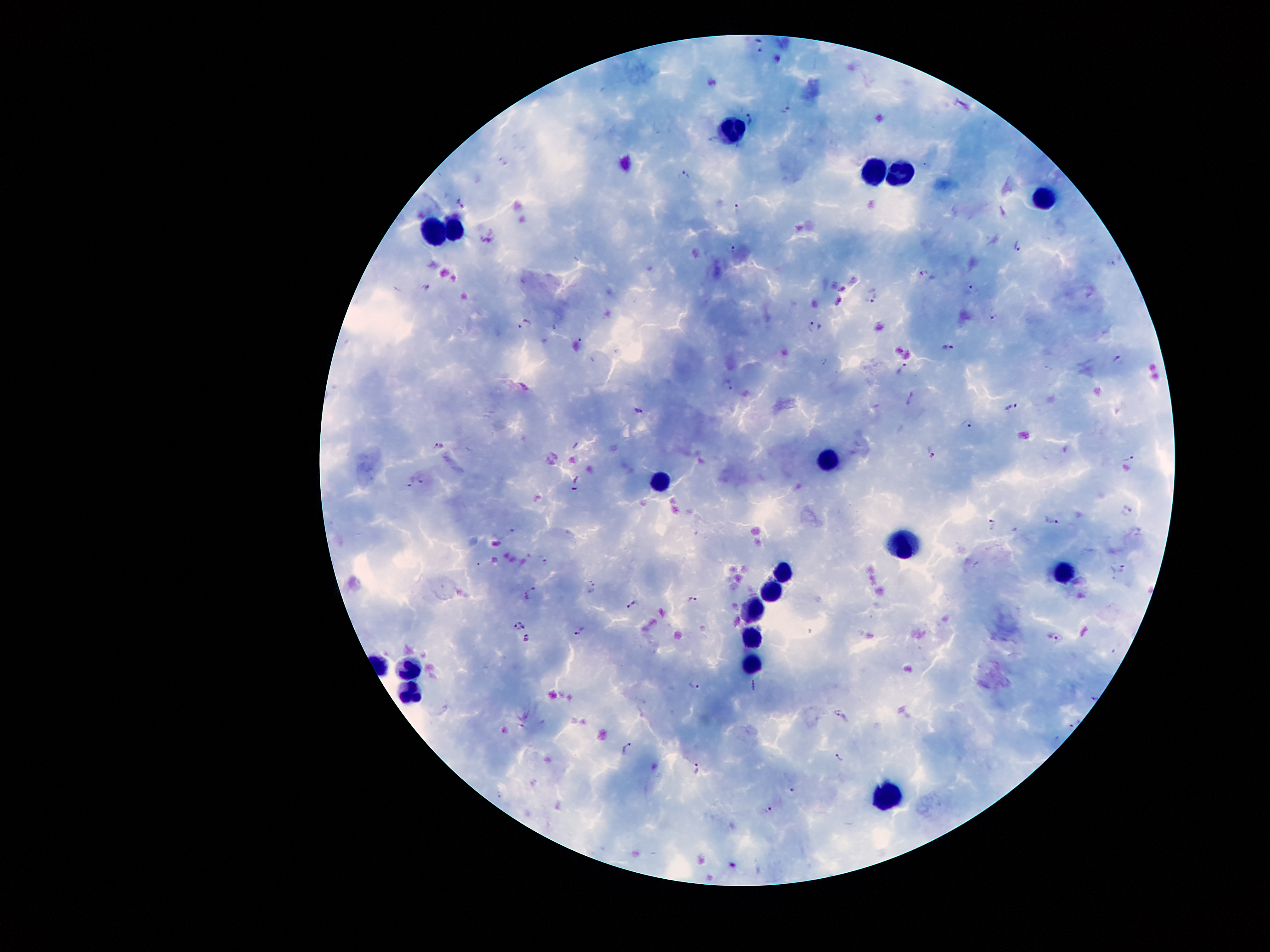 Approximate centers as [x, y] in pixels. Plasmodium parasite locations: [761, 50], [788, 110], [752, 119], [684, 174], [461, 203], [737, 206], [1018, 246], [731, 247], [923, 273], [425, 288], [975, 288], [874, 297], [993, 315], [526, 323], [814, 329], [580, 340], [949, 347], [1118, 360], [902, 369], [729, 383], [1012, 407], [640, 410], [968, 423], [437, 444], [933, 454], [1129, 459], [422, 480], [408, 485], [1126, 511], [1051, 522], [992, 524], [546, 562], [1122, 568], [594, 585], [530, 593], [693, 600], [632, 605], [519, 624], [580, 632], [527, 637], [1059, 638], [693, 684], [1092, 700], [839, 712], [1074, 724], [628, 749], [840, 757], [698, 768], [793, 789], [769, 809]. Leukocyte locations: [731, 126], [903, 164], [870, 169], [1043, 192], [456, 227], [433, 231], [828, 460], [658, 477], [905, 542], [784, 568], [1063, 571], [773, 589], [753, 610], [751, 637], [752, 658], [410, 668], [406, 690], [888, 794]. Image is 1270×952 pixels. Patient malaria status: positive for Plasmodium falciparum. 100x magnification. Giemsa-stained preparation. Single field of view. Thick blood film. Photographed through the microscope eyepiece with a smartphone camera.